Locate every blood parasite and identify its species.
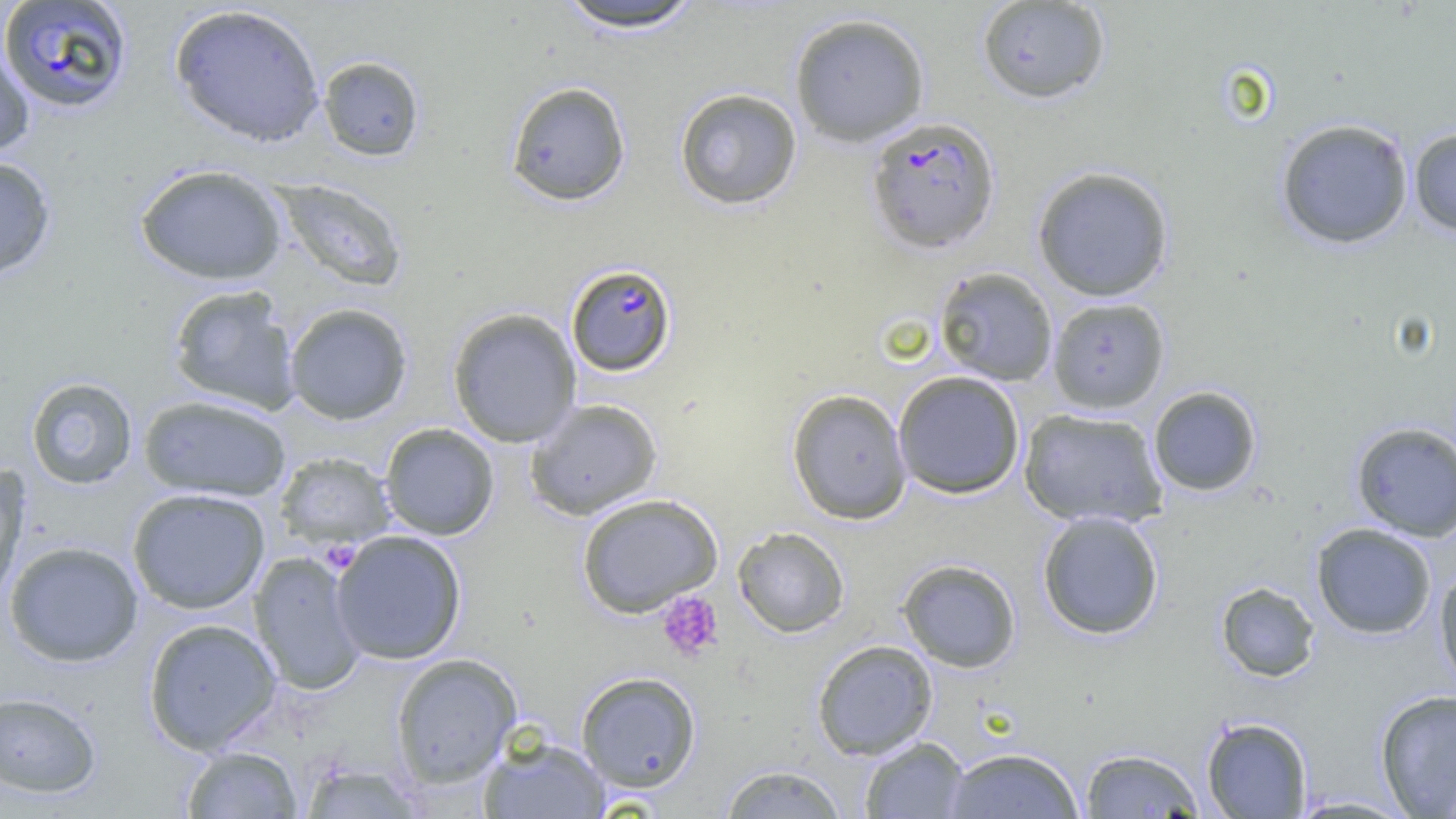
Approximate bounding boxes as [x1, y1, x2, y2] in pixels.
Plasmodium falciparum-infected red blood cells: [0, 0, 133, 114], [865, 116, 1001, 254], [565, 263, 677, 377].
No Plasmodium ovale, Plasmodium malariae, Plasmodium vivax, Babesia divergens, or Trypanosoma brucei observed.

Summary:
  - Platelet locations: [323, 547, 357, 573], [656, 590, 724, 661]
  - Uninfected red blood cell locations: [552, 1, 708, 33], [976, 1, 1112, 104], [169, 3, 326, 148], [788, 11, 930, 147], [0, 43, 35, 157], [317, 55, 425, 162], [505, 81, 631, 207], [674, 87, 803, 210], [1275, 117, 1414, 250], [1408, 127, 1456, 238], [0, 156, 57, 282], [134, 163, 288, 285], [1031, 165, 1175, 302], [272, 177, 409, 293], [934, 266, 1058, 386], [166, 285, 302, 415], [1048, 297, 1170, 414], [284, 302, 413, 425], [447, 307, 582, 448], [892, 370, 1026, 499], [25, 376, 138, 490], [1147, 385, 1262, 497], [786, 388, 912, 524], [137, 394, 292, 503], [524, 398, 663, 520], [1018, 407, 1169, 528], [1350, 420, 1456, 541], [380, 423, 499, 540], [274, 452, 396, 549], [0, 467, 31, 604], [127, 487, 270, 614], [575, 492, 723, 617], [1036, 510, 1165, 640], [1311, 522, 1437, 640], [732, 526, 850, 638], [330, 529, 467, 665], [3, 540, 144, 667], [249, 551, 367, 697], [897, 559, 1022, 673], [1434, 564, 1456, 695], [1215, 581, 1320, 682], [142, 617, 282, 755], [812, 639, 938, 760], [390, 653, 522, 788], [576, 671, 702, 792], [1374, 689, 1456, 817], [0, 690, 102, 798], [1201, 715, 1313, 818], [477, 736, 611, 818], [859, 736, 970, 818], [180, 745, 303, 818], [942, 747, 1085, 818], [1079, 747, 1205, 818], [298, 761, 427, 818], [718, 764, 849, 818], [1287, 794, 1417, 817]
  - Slide-level diagnosis: Plasmodium falciparum
  - Preparation: thin blood film
  - Magnification: 1000x
  - Field of view: one of a larger specimen
  - Image size: 1456×819 pixels
  - Modality: optical microscopy